Report the malaria status of this cell.
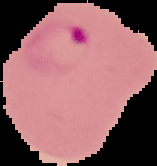
It is parasitized.

From a thin blood smear. The area outside the segmented cell region is set to black. Image is 157×166 pixels.